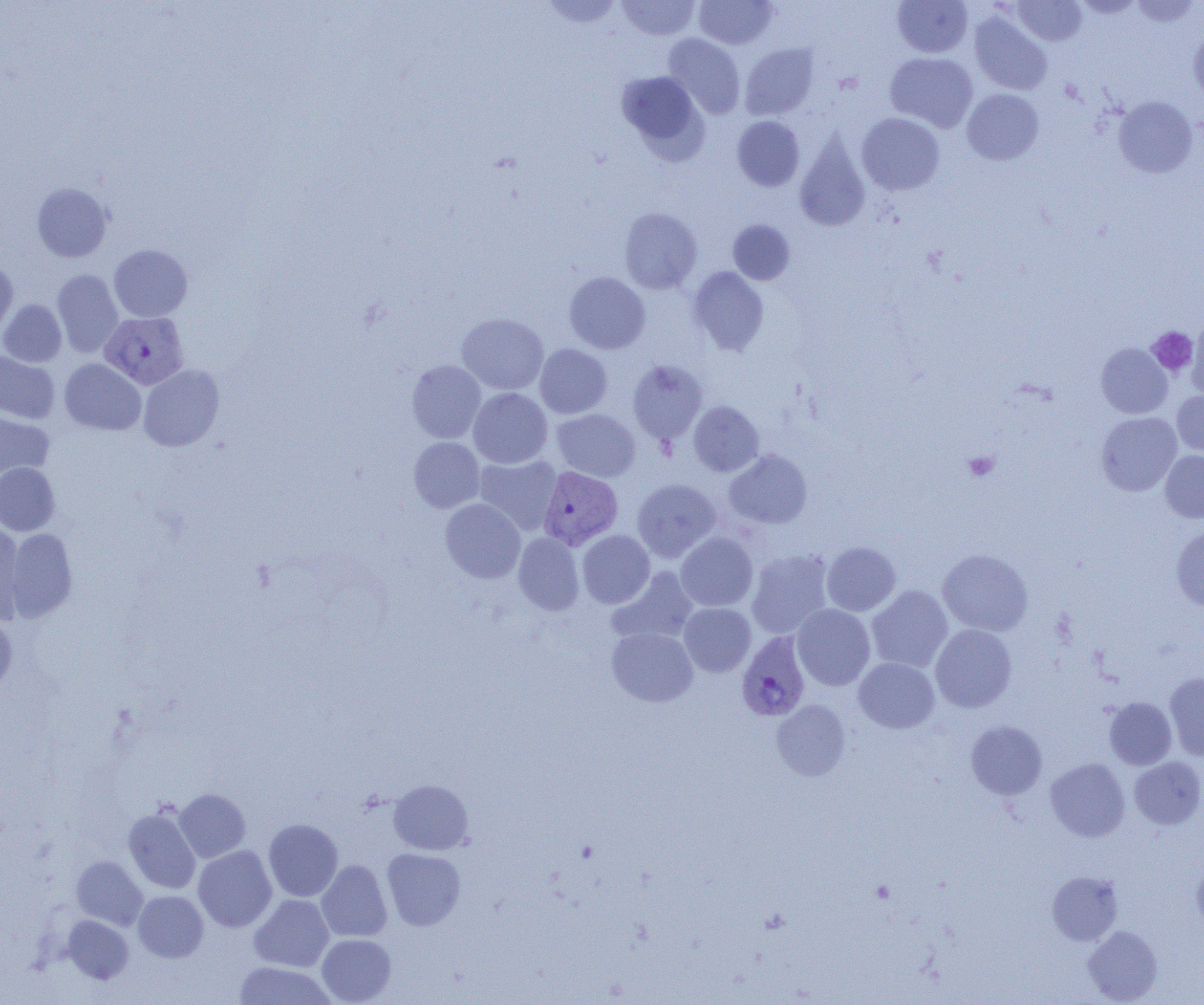

Approximate bounding boxes as [x1, y1, x2, y2] in pixels. Platelet locations: [1147, 326, 1198, 377], [963, 451, 1000, 481]. Plasmodium vivax-infected red blood cell locations: [100, 311, 189, 390], [538, 465, 623, 550], [736, 631, 811, 721]. Uninfected red blood cell locations: [616, 0, 701, 40], [694, 0, 778, 49], [892, 0, 973, 57], [1011, 0, 1087, 46], [1073, 0, 1145, 19], [1131, 0, 1201, 27], [538, 1, 626, 30], [969, 12, 1051, 95], [1188, 29, 1204, 104], [664, 33, 745, 119], [740, 43, 819, 120], [885, 52, 978, 133], [616, 71, 706, 156], [962, 89, 1043, 165], [1113, 96, 1197, 178], [857, 113, 944, 195], [732, 116, 804, 191], [795, 134, 870, 232], [32, 182, 112, 263], [619, 207, 702, 294], [728, 220, 795, 285], [109, 244, 192, 322], [0, 259, 18, 337], [688, 266, 769, 355], [52, 269, 123, 358], [564, 272, 650, 354], [0, 299, 67, 367], [457, 313, 549, 394], [1186, 320, 1204, 399], [1096, 343, 1172, 418], [535, 344, 612, 418], [0, 350, 59, 423], [59, 358, 146, 435], [407, 360, 486, 443], [627, 360, 708, 444], [138, 364, 224, 451], [468, 388, 552, 468], [1172, 391, 1204, 457], [688, 401, 764, 476], [0, 409, 54, 481], [552, 409, 640, 481], [1096, 412, 1182, 496], [409, 437, 485, 513], [724, 449, 812, 529], [1160, 450, 1204, 522], [475, 456, 562, 535], [0, 463, 60, 536], [632, 479, 721, 562], [440, 498, 525, 583], [0, 521, 26, 623], [1171, 525, 1204, 611], [5, 528, 78, 622], [577, 530, 655, 608], [513, 532, 584, 615], [675, 532, 757, 612], [822, 541, 901, 616], [746, 549, 833, 639], [938, 549, 1033, 636], [608, 567, 700, 645], [866, 585, 953, 672], [679, 603, 756, 676], [792, 604, 875, 690], [0, 615, 17, 696], [930, 624, 1017, 712], [607, 627, 698, 706], [854, 657, 939, 733], [1164, 673, 1204, 761], [1105, 697, 1177, 769], [772, 700, 851, 781], [966, 721, 1047, 800], [1130, 756, 1204, 830], [1046, 758, 1130, 842], [388, 780, 473, 854], [174, 788, 250, 862], [123, 807, 201, 894], [263, 819, 343, 901], [193, 845, 277, 932], [381, 848, 466, 930], [71, 856, 148, 930], [316, 860, 392, 942], [1191, 861, 1204, 934], [1047, 871, 1123, 945], [133, 891, 208, 962], [249, 895, 334, 972], [63, 915, 134, 984], [1083, 925, 1162, 1004], [316, 934, 396, 1004], [234, 961, 336, 1004]. Slide-level diagnosis: Plasmodium vivax. 1000x magnification. Optical microscopy. Image is 1204×1005 pixels. One field of a larger specimen. Thin blood smear.